Classify this cell by malaria status.
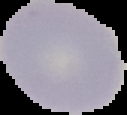
Uninfected.

image_size: 127×115 pixels
image_type: segmented cell region on a black background
preparation: thin blood smear